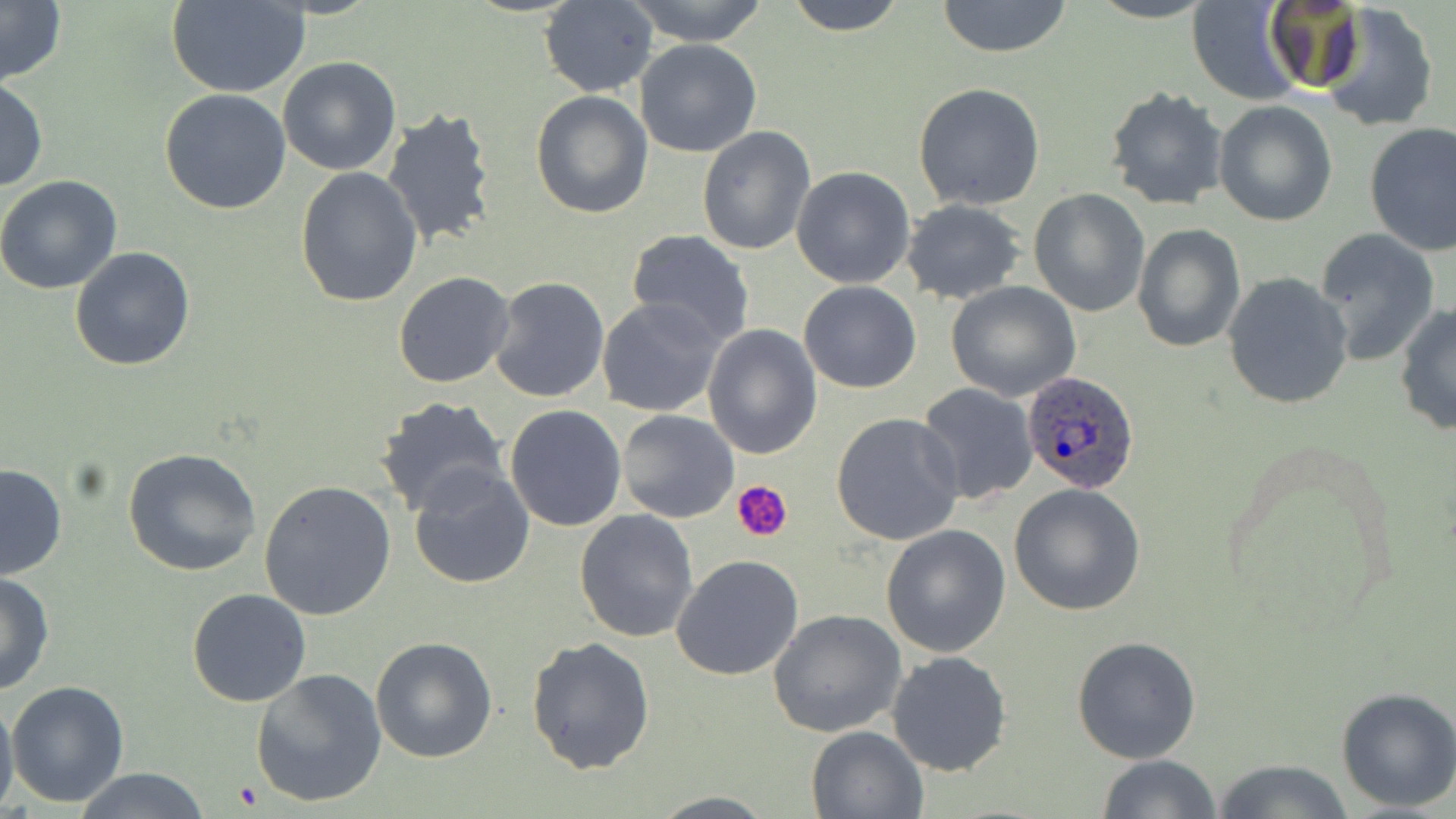
Summary:
  - Coordinate format: approximate bounding boxes as [x1, y1, x2, y2] in pixels
  - Uninfected red blood cell locations: [624, 0, 772, 45], [783, 0, 907, 36], [935, 0, 1074, 57], [1186, 0, 1306, 105], [0, 1, 67, 86], [538, 1, 658, 97], [167, 2, 310, 97], [1259, 2, 1371, 96], [1319, 4, 1440, 131], [635, 39, 762, 156], [277, 56, 402, 175], [0, 76, 46, 192], [912, 83, 1045, 211], [1105, 85, 1230, 211], [159, 87, 292, 214], [531, 90, 653, 219], [1214, 100, 1338, 226], [381, 106, 502, 253], [1363, 121, 1455, 255], [697, 125, 818, 256], [294, 166, 422, 307], [791, 166, 915, 288], [0, 175, 124, 294], [1028, 188, 1150, 317], [900, 199, 1026, 303], [1132, 223, 1246, 352], [1312, 228, 1441, 368], [625, 230, 756, 349], [69, 245, 197, 371], [393, 272, 514, 389], [1223, 272, 1354, 410], [490, 275, 610, 404], [798, 280, 921, 393], [945, 281, 1081, 401], [597, 297, 728, 420], [1394, 303, 1456, 437], [701, 324, 823, 459], [914, 382, 1038, 505], [375, 396, 510, 520], [504, 405, 629, 532], [617, 410, 739, 523], [831, 411, 965, 545], [122, 447, 262, 577], [406, 462, 536, 589], [0, 464, 68, 581], [259, 481, 396, 620], [1010, 483, 1147, 615], [575, 509, 699, 642], [882, 525, 1011, 657], [670, 555, 803, 680], [0, 573, 55, 696], [186, 589, 312, 708], [768, 609, 906, 739], [1071, 634, 1203, 764], [369, 635, 498, 762], [526, 637, 656, 775], [886, 650, 1012, 777], [249, 669, 387, 808], [6, 680, 129, 808], [1334, 686, 1456, 812], [0, 691, 19, 819], [805, 724, 929, 817], [1095, 754, 1225, 818], [1209, 760, 1360, 817], [69, 768, 211, 819], [648, 792, 778, 818]
  - Plasmodium ovale-infected red blood cell locations: [1021, 370, 1139, 494]
  - Platelet locations: [734, 481, 793, 543], [231, 782, 265, 809]
  - Slide-level diagnosis: Plasmodium ovale
  - Preparation: thin blood smear
  - Field of view: single
  - Image size: 1456×819 pixels
  - Modality: light microscopy
  - Magnification: 1000x
  - Stain: May-Grünwald-Giemsa